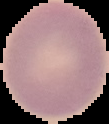

image type = segmented cell region on a black background
image size = 109×124 pixels
preparation = thin blood film
result = negative for Plasmodium parasites